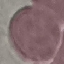 Malaria status: uninfected. Photographed with a smartphone camera at the microscope eyepiece. Thin smear of blood. Cell patch, automatically extracted from a larger field of view and resized to 64 × 64 pixels. Giemsa-stained preparation.